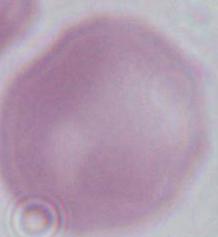
identification = erythrocyte
magnification = 1000x
modality = photomicrograph